Assess this cell for malaria.
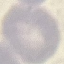
Uninfected.

Summary:
  - Preparation: thin smear
  - Image type: automatically extracted cell patch, resized to 64 × 64 pixels
  - Capture: smartphone through the microscope eyepiece
  - Stain: Giemsa